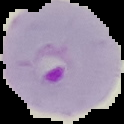

{
  "image_type": "segmented cell region on a black background",
  "preparation": "thin blood film",
  "image_size": "124×124 pixels",
  "result": "Plasmodium parasites detected"
}